Assess the morphology of the erythrocytes.
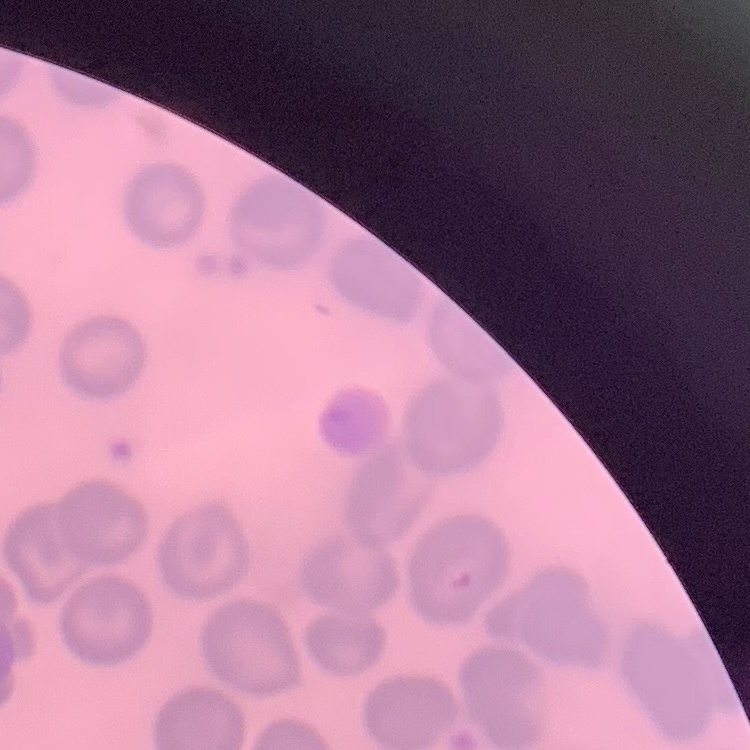
No rouleaux formation.

Thin blood smear. Field's or Giemsa stain. Square crop of a larger photomicrograph.